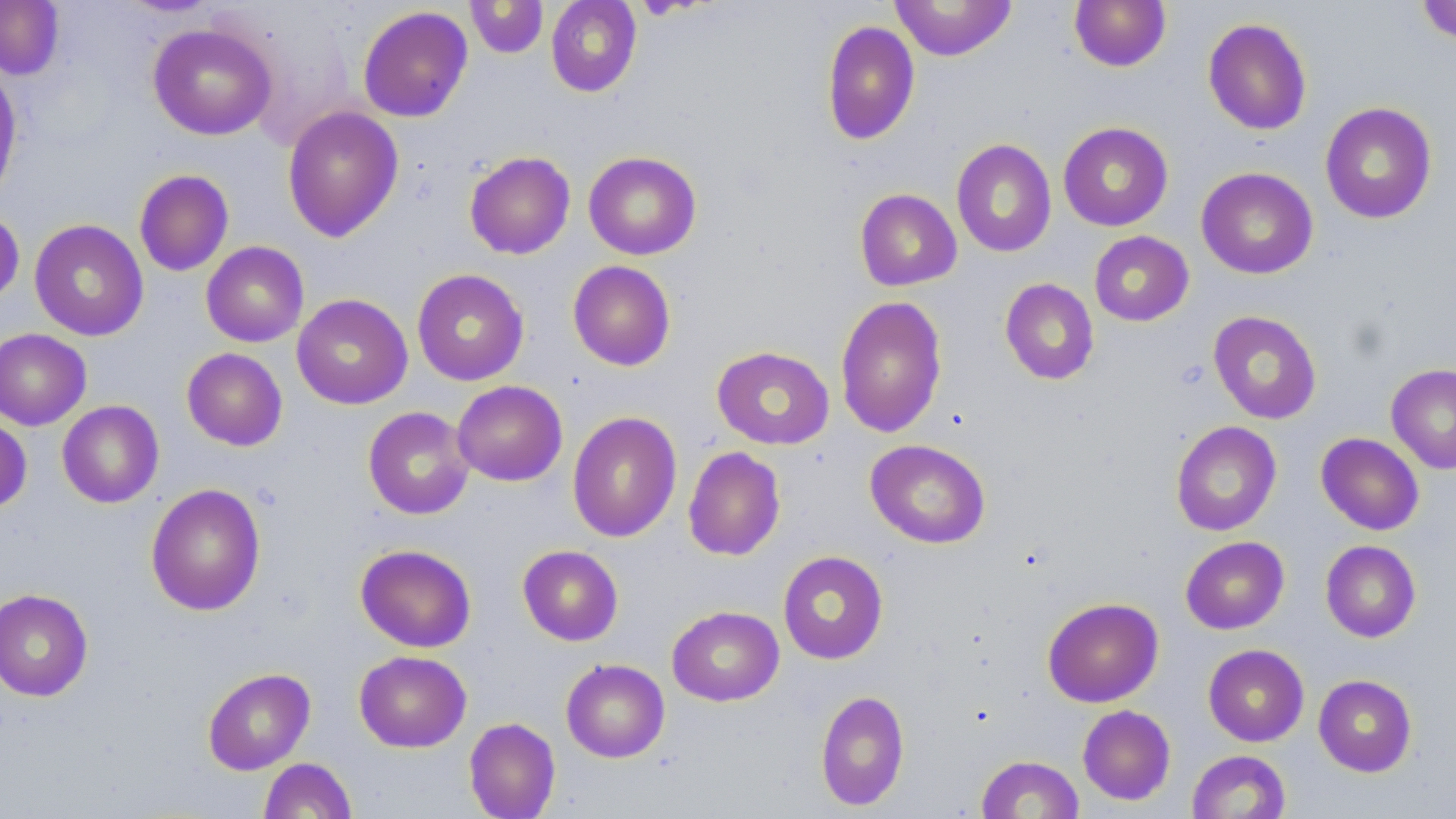
Summary:
  - Coordinate format: approximate bounding boxes as [x1, y1, x2, y2] in pixels
  - Uninfected red blood cell locations: [465, 0, 549, 59], [546, 0, 641, 97], [1069, 0, 1171, 72], [1415, 0, 1456, 45], [0, 1, 64, 79], [889, 1, 1017, 61], [357, 6, 473, 123], [1202, 17, 1312, 136], [821, 19, 920, 146], [147, 23, 277, 140], [0, 60, 23, 207], [1319, 102, 1438, 224], [282, 106, 403, 242], [1058, 121, 1173, 231], [951, 139, 1057, 257], [464, 150, 576, 259], [583, 151, 702, 260], [1196, 167, 1318, 279], [134, 169, 234, 276], [854, 189, 961, 291], [0, 209, 24, 306], [29, 219, 149, 341], [1089, 231, 1194, 326], [201, 241, 309, 347], [567, 260, 676, 371], [412, 269, 529, 386], [1000, 278, 1099, 385], [292, 294, 413, 409], [834, 295, 948, 438], [1207, 310, 1322, 424], [0, 328, 91, 430], [712, 345, 834, 450], [181, 348, 287, 451], [1386, 363, 1456, 474], [452, 380, 567, 486], [57, 400, 164, 508], [363, 407, 474, 520], [567, 411, 683, 543], [0, 414, 32, 513], [1170, 421, 1282, 536], [1316, 432, 1425, 535], [865, 439, 990, 548], [683, 446, 785, 561], [145, 483, 266, 616], [1180, 536, 1289, 634], [1320, 540, 1421, 643], [355, 544, 477, 652], [517, 545, 623, 646], [777, 550, 889, 665], [0, 588, 93, 702], [1042, 597, 1164, 708], [667, 606, 784, 706], [1203, 644, 1309, 746], [354, 650, 472, 752], [561, 659, 670, 762], [202, 668, 316, 775], [1313, 674, 1417, 777], [815, 689, 910, 811], [1078, 705, 1176, 805], [464, 717, 561, 818], [1186, 750, 1291, 819], [976, 754, 1084, 818], [258, 758, 357, 819]
  - Slide-level diagnosis: negative for blood parasites
  - Image size: 1456×819 pixels
  - Field of view: single
  - Preparation: thin blood film
  - Stain: May-Grünwald-Giemsa
  - Magnification: 1000x
  - Modality: optical microscopy